Assess for malaria.
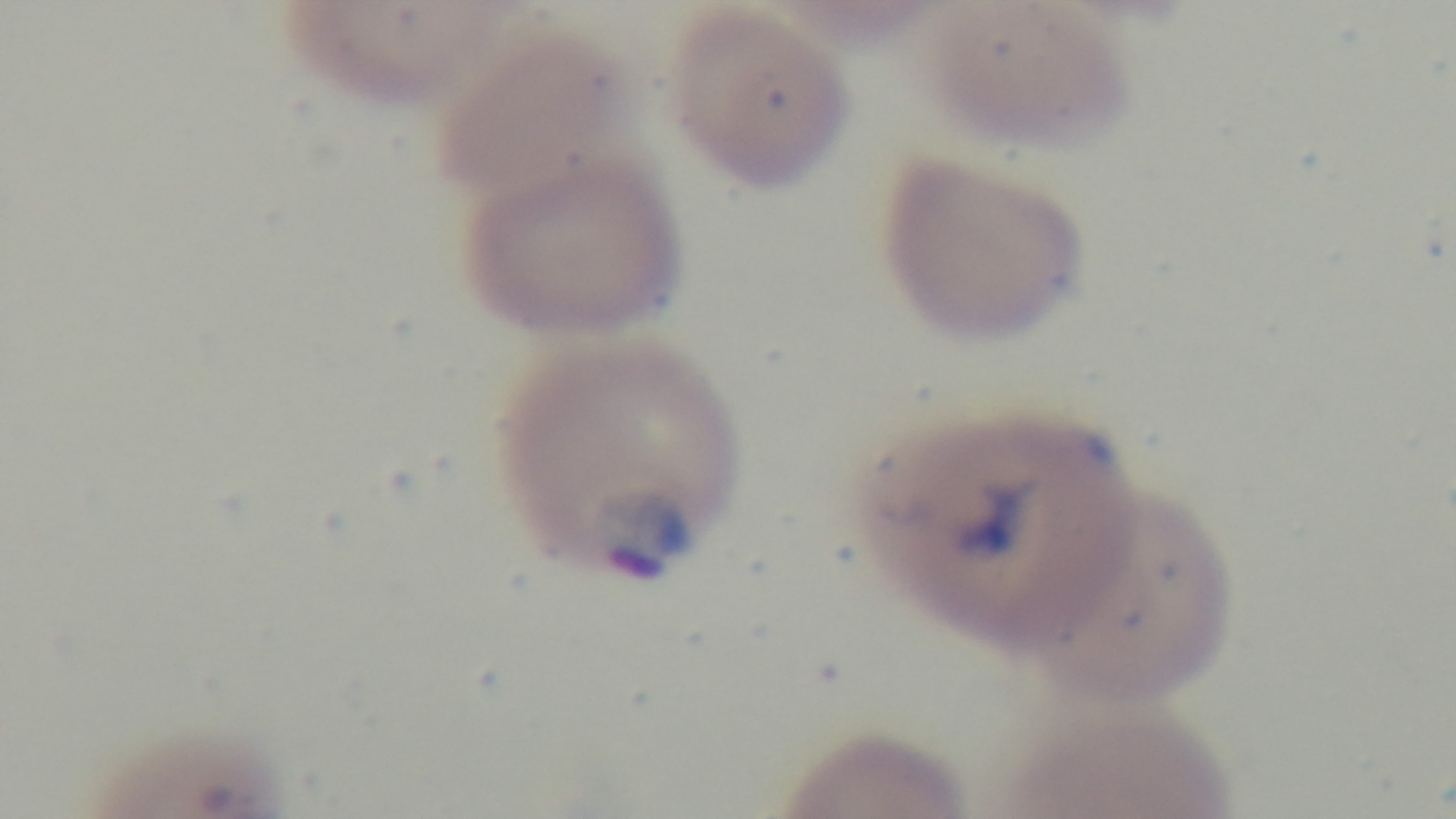

Infected.

field_of_view: one from the slide
objective: 100x oil immersion
modality: light microscopy
stain: Giemsa
preparation: thin
capture: mounted 4K digital camera